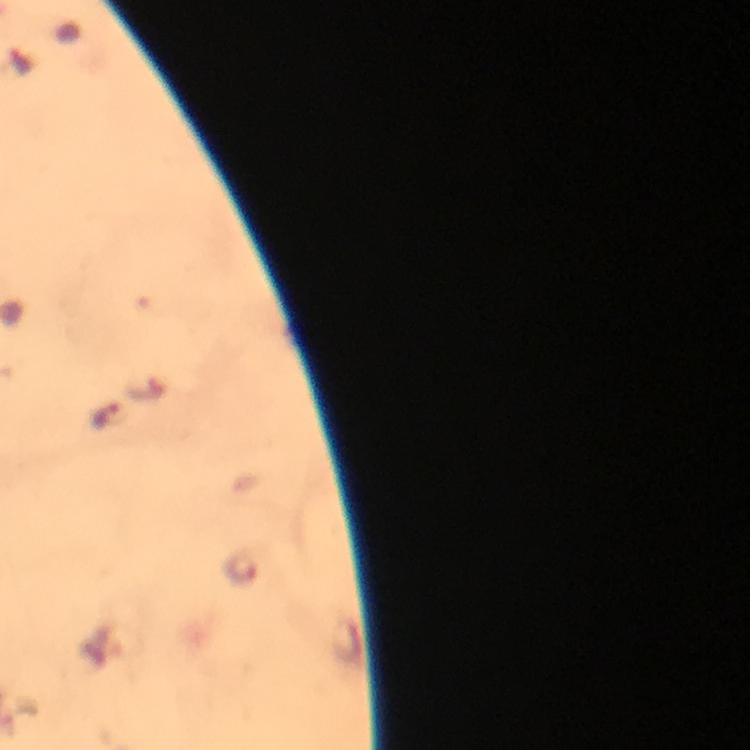 Approximate centers as {x, y} in pixels. Plasmodium parasite locations: {108, 416}. At 100x magnification. From a malaria diagnostic workup. Thick smear. Cropped region of a single field of view. Immersion oil was used. Image is 750×750 pixels. Smartphone photograph taken through a microscope. Giemsa stain.